Name the cell type shown.
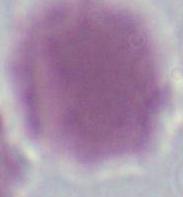
This is an erythrocyte.

Summary:
  - Modality: photomicrograph
  - Magnification: 1000x